Point out every malaria parasite and every leukocyte.
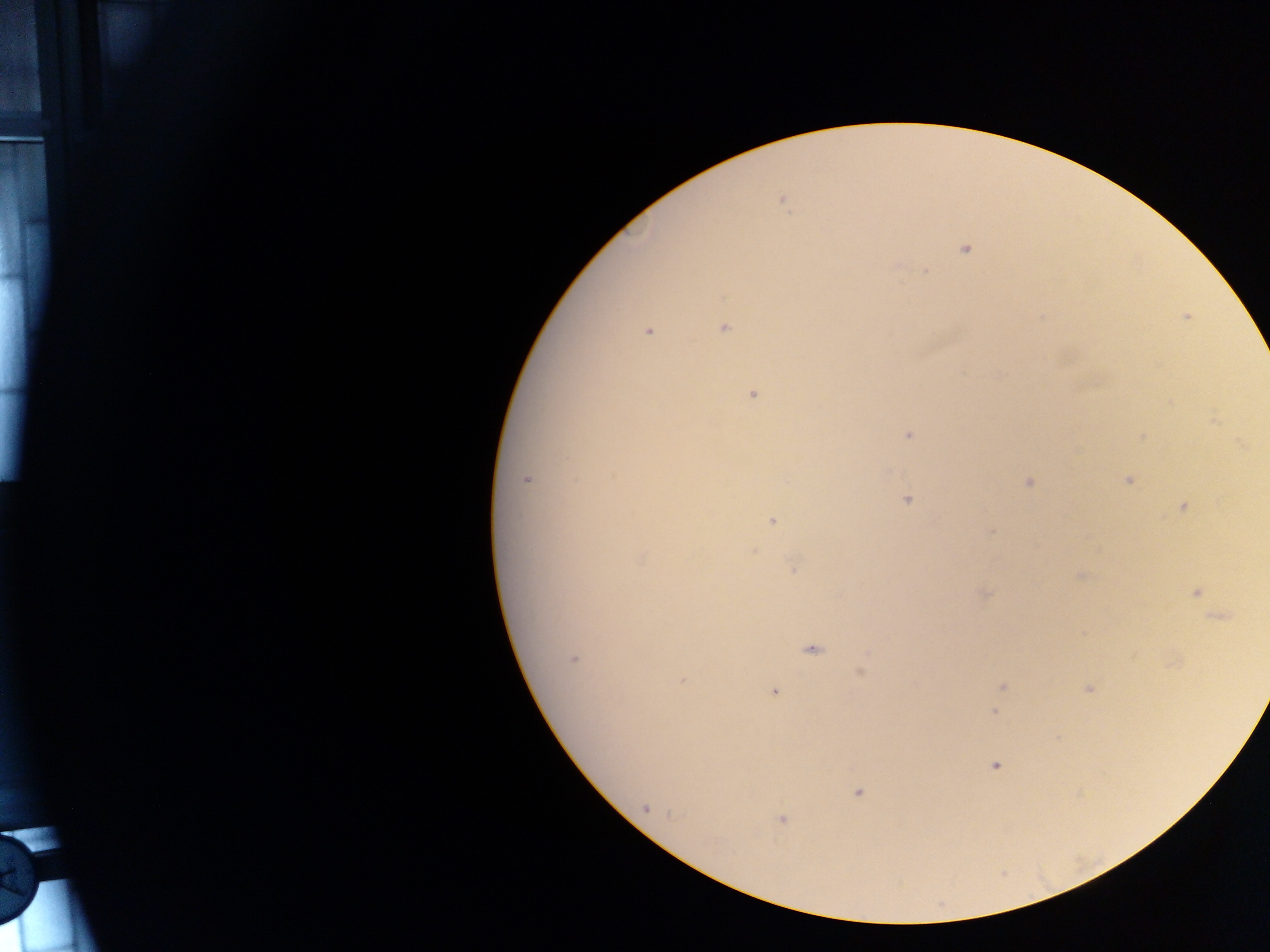
Approximate centers as [x, y] in pixels.
Malaria parasites: [782, 200], [965, 248], [925, 271], [1186, 317], [1042, 318], [724, 328], [648, 332], [753, 395], [1215, 420], [908, 434], [1141, 437], [527, 479], [1128, 480], [1028, 483], [906, 500], [1184, 506], [772, 521], [991, 531], [754, 551], [794, 569], [1080, 576], [1196, 592], [986, 594], [1221, 618], [811, 650], [573, 659], [860, 673], [682, 681], [1002, 687], [1089, 689], [774, 691], [995, 712], [995, 766], [858, 793], [646, 809], [781, 818].
No leukocytes observed.

preparation = thick blood film
field of view = single
capture = mobile-phone photograph through a microscope
image size = 1270×952 pixels
country = Ghana